Classify this cell by malaria status.
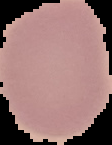

Uninfected.

{
  "image_size": "112×145 pixels",
  "preparation": "thin blood film",
  "image_type": "segmented cell region on a black background"
}